Outline each blood parasite and name the species.
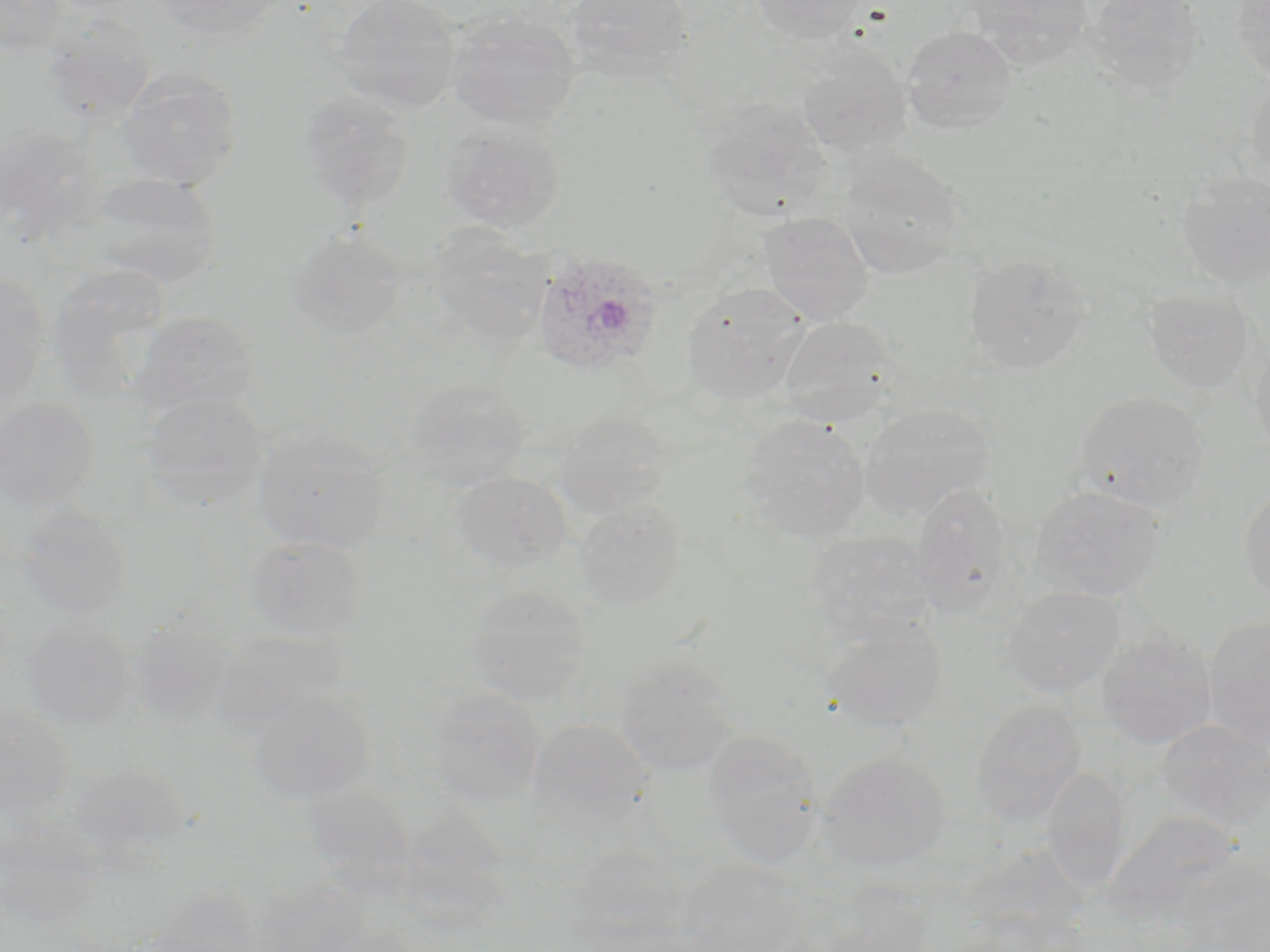

Approximate bounding boxes as (x1, y1, x2, y2) in pixels.
Plasmodium ovale-infected red blood cells: (531, 252, 663, 377).
No Plasmodium falciparum, Plasmodium malariae, Plasmodium vivax, Babesia divergens, or Trypanosoma brucei observed.

slide_level_diagnosis: Plasmodium ovale
preparation: thin blood film
image_size: 1270×952 pixels
stain: May-Grünwald-Giemsa
magnification: 1000x
modality: optical microscopy
field_of_view: one of a larger specimen
uninfected_red_blood_cell_locations: 'approximate bounding boxes as (x1, y1, x2, y2) in pixels: (0, 0, 69, 57), (43, 0, 154, 16), (153, 0, 289, 39), (334, 0, 461, 113), (567, 0, 693, 80), (751, 0, 866, 44), (966, 0, 1093, 66), (1091, 0, 1203, 90), (1234, 0, 1270, 84), (448, 11, 579, 128), (39, 14, 155, 124), (903, 25, 1017, 132), (797, 48, 910, 155), (118, 68, 242, 188), (1247, 76, 1270, 185), (298, 91, 414, 213), (702, 100, 831, 220), (441, 122, 564, 231), (0, 123, 101, 243), (836, 151, 963, 278), (87, 171, 223, 287), (1179, 172, 1270, 287), (758, 211, 876, 323), (432, 227, 552, 344), (288, 229, 404, 340), (964, 253, 1090, 372), (47, 264, 173, 398), (0, 271, 50, 407), (682, 285, 811, 404), (1142, 288, 1255, 392), (132, 311, 258, 416), (777, 315, 899, 424), (1250, 338, 1270, 459), (405, 378, 529, 488), (1075, 390, 1210, 512), (140, 391, 269, 504), (0, 397, 99, 511), (859, 404, 994, 519), (555, 410, 672, 517), (739, 414, 870, 539), (253, 428, 391, 553), (452, 471, 570, 572), (1240, 482, 1270, 606), (911, 484, 1014, 614), (1030, 485, 1166, 600), (574, 498, 685, 610), (16, 504, 133, 620), (804, 531, 935, 637), (245, 536, 369, 640), (466, 585, 590, 705), (1002, 586, 1124, 696), (126, 614, 234, 723), (23, 615, 137, 731), (1203, 616, 1270, 746), (823, 620, 946, 730), (209, 631, 350, 733), (1096, 633, 1217, 748), (613, 654, 737, 775), (425, 687, 546, 805), (246, 691, 376, 804), (971, 699, 1085, 824), (0, 704, 73, 822), (527, 718, 651, 825), (1157, 718, 1270, 827), (703, 729, 822, 865), (817, 751, 949, 870), (69, 762, 192, 862), (1042, 765, 1131, 894), (302, 784, 416, 890), (0, 811, 102, 926), (566, 847, 688, 945), (677, 863, 804, 951), (821, 878, 933, 951), (252, 881, 370, 952), (140, 885, 265, 951)'